Assess this cell for malaria.
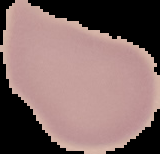
Uninfected.

Image is 160×154 pixels. Cell region segmented out of the field of view; the surrounding area is masked to black. From a thin blood film.